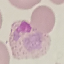

Summary:
  - Result: malaria parasites identified
  - Stain: Giemsa
  - Preparation: thin smear
  - Capture: smartphone through the microscope eyepiece
  - Image type: cell patch, automatically extracted from a larger field of view and resized to 64 × 64 pixels